Outline every Plasmodium parasite, every leukocyte, and every artifact (stain precipitate or debris).
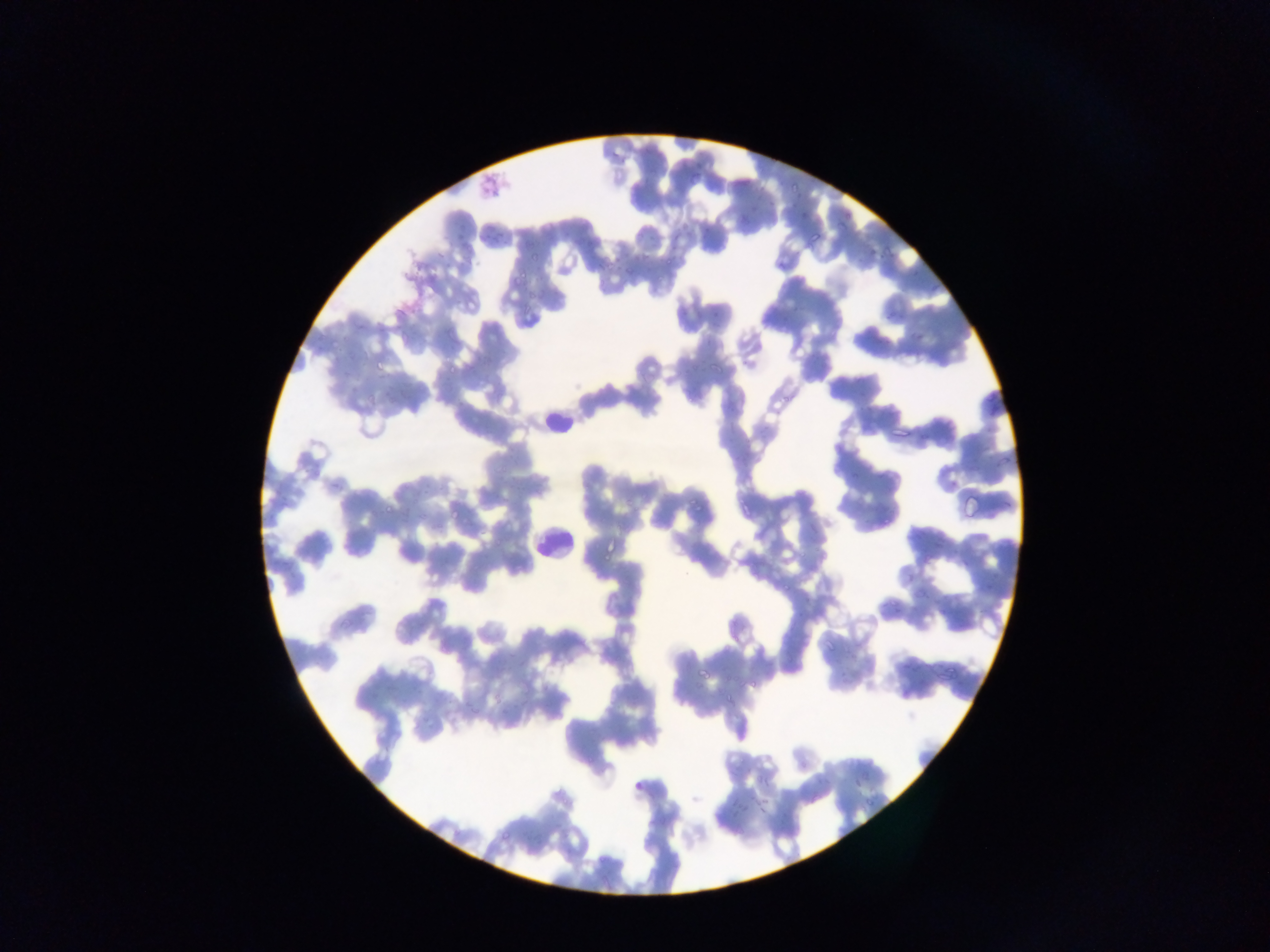
Approximate bounding boxes as left top right bottom in pixels.
Plasmodium parasites: 455 217 476 241; 520 227 543 250; 490 228 502 242; 575 236 596 253; 808 240 828 244; 438 246 461 272; 591 259 615 279; 515 271 532 290; 908 320 936 341; 1001 453 1015 465; 1002 478 1019 512; 688 495 709 518; 881 511 898 527; 905 566 924 585; 978 576 999 598; 779 579 793 591; 932 590 951 609; 693 667 709 678; 748 676 757 689; 720 696 731 708; 760 769 775 783; 632 774 647 798; 849 778 867 788; 805 789 831 810; 861 796 877 813; 729 801 748 823; 757 801 774 818.
Leukocytes: 540 382 574 435; 534 526 570 561.

image size = 1270×952 pixels
capture = mobile-phone photograph through a microscope
country = Ghana
preparation = thin blood smear
field of view = single